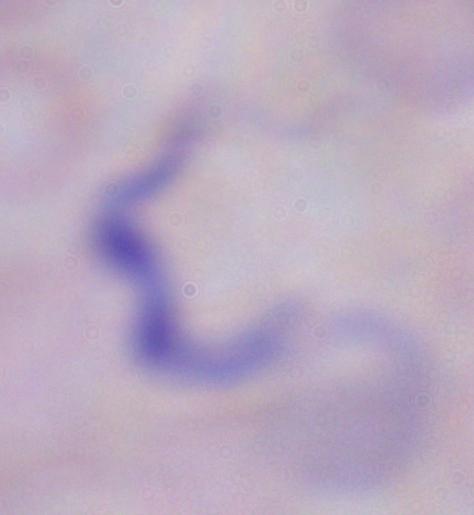
Summary:
  - Modality: photomicrograph
  - Magnification: 1000x
  - Identification: trypanosome